Evaluate for Plasmodium parasites.
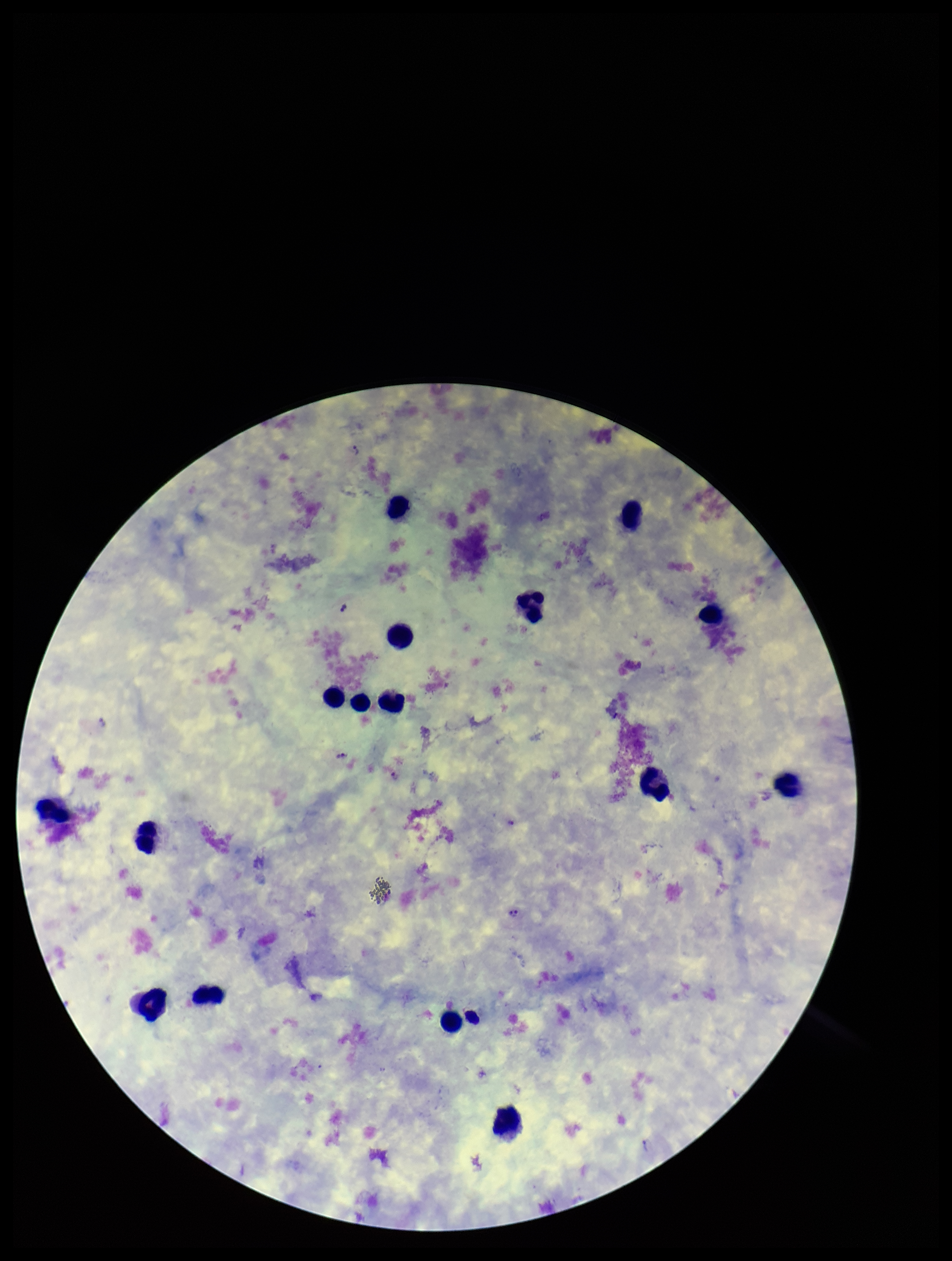
Detected.

capture: smartphone photograph through the microscope eyepiece
stain: Giemsa
field_of_view: single
preparation: thick blood smear
leukocyte_count: 16
image_size: 952×1261 pixels
species_reported_for_this_patient: Plasmodium vivax
parasite_count: 4
patient_malaria_status: positive